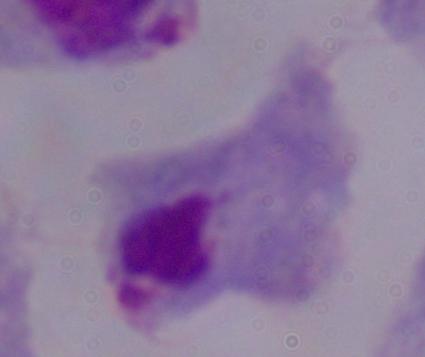
Micrograph. 1000x magnification. A trichomonad is shown.